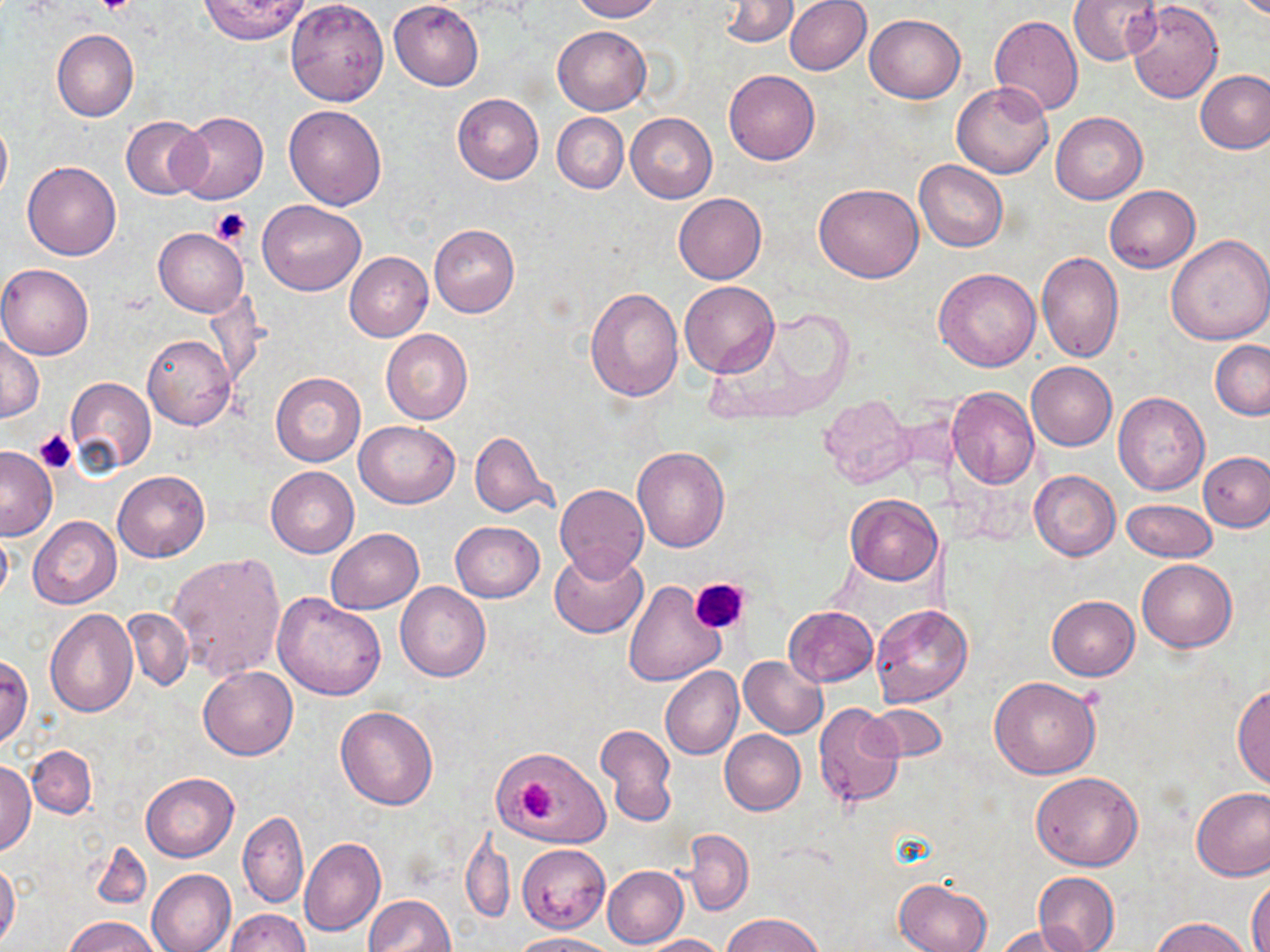 Approximate bounding boxes as (x1, y1, x2, y2) in pixels. Uninfected red blood cell locations: (199, 0, 310, 44), (285, 0, 390, 105), (388, 0, 483, 91), (567, 0, 662, 22), (785, 0, 871, 75), (1067, 0, 1160, 66), (719, 1, 799, 46), (1128, 1, 1223, 103), (865, 14, 965, 103), (991, 16, 1082, 116), (552, 25, 651, 115), (52, 29, 138, 122), (724, 69, 820, 165), (1196, 70, 1270, 154), (951, 81, 1054, 178), (452, 93, 544, 184), (283, 104, 387, 209), (1051, 111, 1147, 203), (626, 112, 717, 202), (173, 113, 267, 204), (553, 113, 629, 193), (0, 115, 11, 205), (120, 117, 209, 198), (915, 160, 1007, 252), (22, 161, 121, 260), (814, 182, 923, 283), (1104, 185, 1199, 272), (673, 193, 765, 284), (257, 200, 366, 295), (429, 224, 519, 317), (153, 228, 248, 318), (1164, 234, 1270, 346), (344, 251, 433, 341), (1037, 251, 1124, 363), (0, 264, 93, 359), (934, 267, 1041, 372), (678, 281, 779, 378), (585, 284, 682, 403), (701, 309, 853, 422), (381, 328, 473, 424), (0, 334, 43, 422), (142, 334, 236, 430), (1211, 340, 1270, 419), (1027, 361, 1117, 450), (271, 370, 365, 467), (65, 377, 156, 473), (948, 386, 1039, 488), (1114, 392, 1209, 495), (818, 395, 913, 488), (355, 422, 460, 508), (468, 430, 558, 519), (1, 445, 57, 540), (633, 447, 729, 552), (1199, 451, 1270, 532), (266, 466, 359, 558), (113, 470, 210, 562), (1029, 470, 1120, 560), (554, 485, 648, 580), (845, 494, 943, 586), (1123, 498, 1216, 562), (28, 516, 121, 608), (450, 521, 544, 602), (0, 524, 13, 609), (325, 528, 423, 613), (549, 548, 647, 638), (169, 551, 286, 681), (1137, 558, 1238, 653), (624, 579, 727, 685), (396, 581, 491, 682), (272, 592, 386, 700), (1047, 596, 1139, 680), (870, 604, 973, 708), (784, 606, 878, 687), (123, 608, 193, 691), (44, 609, 137, 716), (0, 655, 33, 746), (738, 655, 827, 738), (198, 665, 298, 760), (660, 666, 744, 760), (988, 676, 1100, 779), (1233, 684, 1270, 791), (814, 703, 907, 809), (868, 703, 946, 762), (335, 705, 439, 810), (596, 723, 677, 827), (720, 731, 806, 815), (26, 746, 97, 817), (493, 747, 608, 846), (1, 760, 36, 853), (1030, 771, 1144, 870), (140, 773, 238, 861), (1191, 786, 1270, 881), (238, 811, 309, 908), (463, 824, 514, 923), (680, 828, 753, 916), (299, 836, 385, 936), (88, 840, 151, 911), (517, 844, 611, 932), (0, 860, 21, 947), (602, 865, 688, 949), (146, 868, 236, 952), (1033, 871, 1120, 952), (1248, 874, 1270, 952), (894, 877, 992, 952), (364, 894, 454, 952), (224, 908, 309, 952), (721, 913, 824, 952), (1149, 915, 1254, 952), (66, 916, 161, 952), (995, 923, 1093, 951), (511, 932, 617, 952), (638, 934, 725, 951). Platelet locations: (96, 0, 136, 17), (211, 207, 252, 245), (33, 429, 78, 473), (692, 578, 750, 635), (517, 779, 558, 820). Slide-level diagnosis: negative for blood parasites. 1000x magnification. Thin blood film. May-Grünwald-Giemsa-stained preparation. Optical microscopy. Image is 1270×952 pixels. Single field of view.